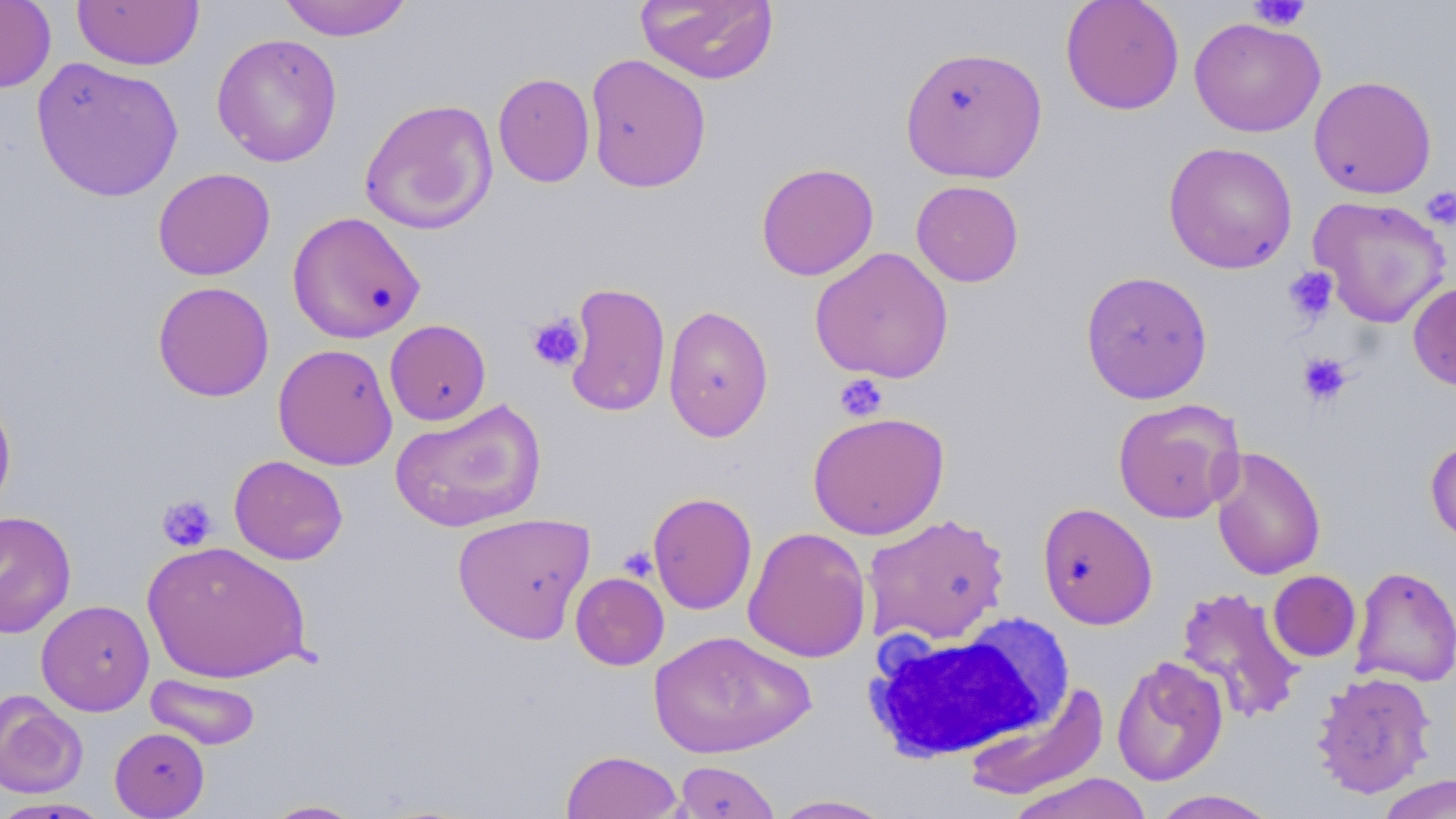
Approximate bounding boxes as named x1/y1/x2/y2 corners in pixels. Platelet locations: (x1=1247, y1=1, x2=1311, y2=31), (x1=1423, y1=187, x2=1456, y2=230), (x1=1283, y1=266, x2=1338, y2=324), (x1=527, y1=313, x2=586, y2=372), (x1=1297, y1=352, x2=1352, y2=407), (x1=835, y1=373, x2=888, y2=421), (x1=157, y1=494, x2=218, y2=551), (x1=618, y1=546, x2=658, y2=582). Uninfected red blood cell locations: (x1=0, y1=0, x2=56, y2=93), (x1=277, y1=0, x2=414, y2=41), (x1=635, y1=0, x2=779, y2=85), (x1=1060, y1=0, x2=1185, y2=115), (x1=72, y1=1, x2=205, y2=70), (x1=1189, y1=16, x2=1325, y2=137), (x1=211, y1=33, x2=343, y2=167), (x1=899, y1=44, x2=1048, y2=183), (x1=585, y1=53, x2=712, y2=193), (x1=31, y1=57, x2=184, y2=202), (x1=493, y1=72, x2=595, y2=187), (x1=1308, y1=75, x2=1437, y2=199), (x1=359, y1=98, x2=498, y2=235), (x1=1163, y1=141, x2=1298, y2=274), (x1=756, y1=162, x2=879, y2=281), (x1=152, y1=167, x2=275, y2=280), (x1=911, y1=180, x2=1024, y2=287), (x1=1308, y1=195, x2=1451, y2=328), (x1=287, y1=211, x2=426, y2=343), (x1=809, y1=246, x2=954, y2=383), (x1=1080, y1=269, x2=1213, y2=403), (x1=152, y1=281, x2=274, y2=402), (x1=1408, y1=281, x2=1456, y2=391), (x1=563, y1=282, x2=671, y2=417), (x1=662, y1=304, x2=774, y2=443), (x1=385, y1=319, x2=491, y2=425), (x1=273, y1=343, x2=398, y2=470), (x1=0, y1=390, x2=17, y2=515), (x1=389, y1=398, x2=547, y2=533), (x1=1111, y1=398, x2=1244, y2=525), (x1=807, y1=411, x2=949, y2=539), (x1=1425, y1=436, x2=1456, y2=545), (x1=1209, y1=446, x2=1326, y2=581), (x1=228, y1=455, x2=348, y2=565), (x1=647, y1=491, x2=758, y2=615), (x1=1037, y1=502, x2=1158, y2=629), (x1=0, y1=510, x2=76, y2=639), (x1=451, y1=512, x2=596, y2=644), (x1=862, y1=513, x2=1011, y2=645), (x1=743, y1=526, x2=872, y2=663), (x1=141, y1=541, x2=311, y2=684), (x1=1350, y1=566, x2=1456, y2=687), (x1=1268, y1=570, x2=1361, y2=662), (x1=570, y1=572, x2=669, y2=670), (x1=1174, y1=585, x2=1306, y2=723), (x1=36, y1=599, x2=154, y2=715), (x1=648, y1=630, x2=817, y2=759), (x1=1111, y1=655, x2=1229, y2=787), (x1=1311, y1=670, x2=1436, y2=798), (x1=146, y1=673, x2=261, y2=749), (x1=965, y1=684, x2=1110, y2=801), (x1=0, y1=692, x2=88, y2=798), (x1=109, y1=726, x2=210, y2=818), (x1=560, y1=750, x2=684, y2=818), (x1=673, y1=760, x2=780, y2=819), (x1=1004, y1=772, x2=1154, y2=819), (x1=1376, y1=774, x2=1456, y2=818), (x1=1148, y1=789, x2=1279, y2=818), (x1=769, y1=795, x2=895, y2=818), (x1=0, y1=796, x2=114, y2=818), (x1=260, y1=799, x2=367, y2=818). White blood cell locations: (x1=862, y1=623, x2=1060, y2=762). Slide-level diagnosis: negative for blood parasites. Single field of view. May-Grünwald-Giemsa-stained preparation. Light microscopy. 1000x magnification. Image is 1456×819 pixels. Thin blood smear.